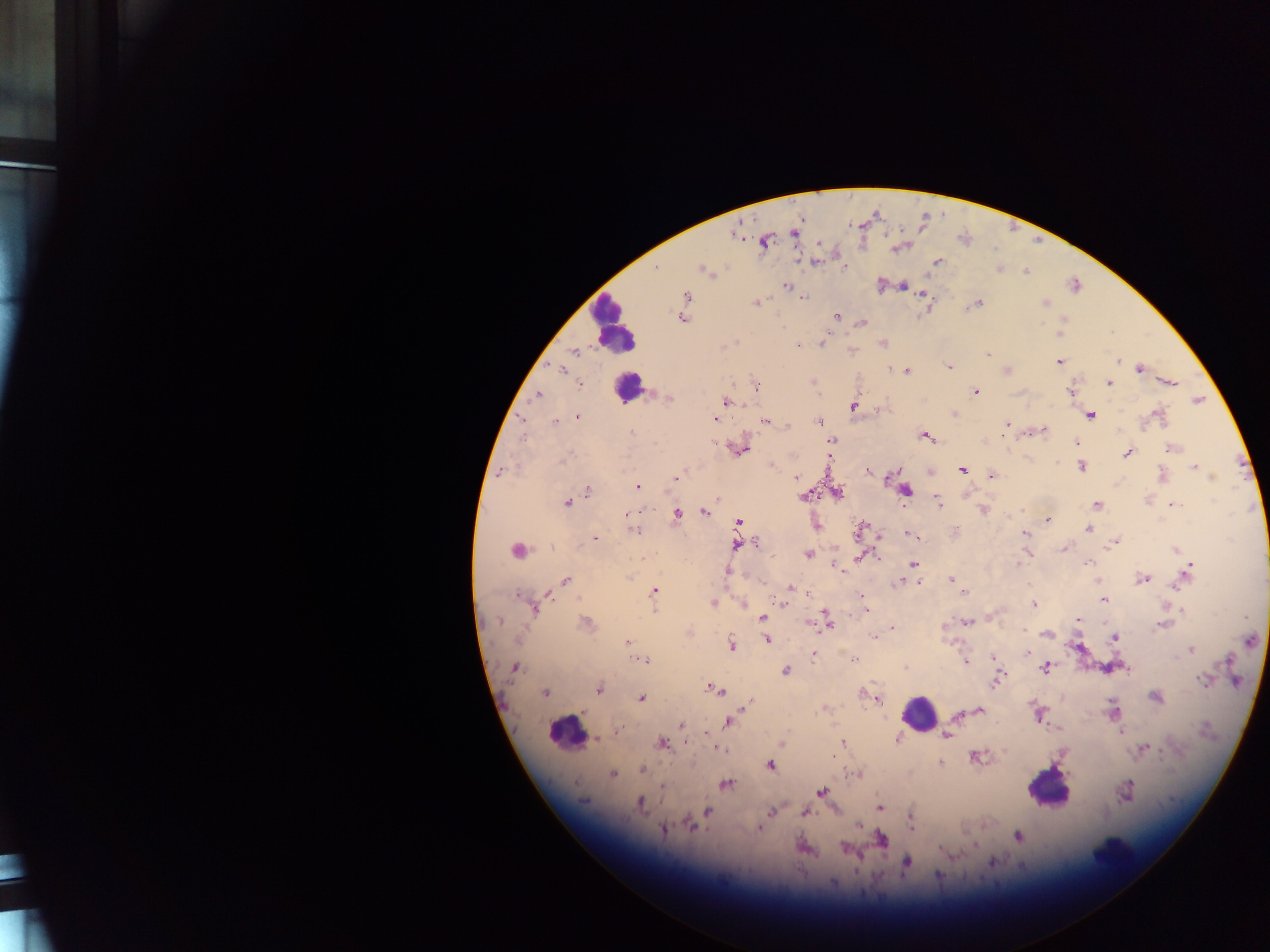

Approximate centers as (x, y) in pixels.
Summary:
  - Leukocyte locations: (613, 325), (628, 388), (919, 714), (565, 729), (1047, 788)
  - Plasmodium parasite locations: (794, 233), (764, 242), (897, 248), (815, 261), (937, 261), (844, 267), (657, 268), (704, 270), (1026, 271), (786, 286), (1076, 286), (904, 287), (923, 295), (686, 296), (804, 298), (755, 303), (978, 303), (1045, 303), (836, 316), (682, 318), (862, 323), (783, 327), (1059, 334), (733, 343), (882, 343), (822, 344), (797, 346), (723, 347), (852, 350), (575, 351), (987, 354), (1118, 362), (1058, 363), (948, 366), (1139, 368), (562, 369), (1006, 370), (907, 371), (813, 381), (1170, 381), (1109, 383), (580, 384), (756, 386), (1072, 390), (975, 392), (537, 394), (669, 398), (1197, 400), (727, 402), (854, 407), (955, 414), (1092, 415), (577, 416), (1158, 416), (522, 418), (715, 419), (819, 421), (555, 422), (767, 422), (787, 425), (1005, 427), (1043, 430), (632, 433), (1003, 433), (522, 436), (926, 436), (832, 441), (1076, 443), (1171, 448), (741, 449), (1127, 453), (831, 457), (564, 458), (1081, 467), (1193, 467), (867, 470), (963, 470), (502, 472), (1162, 474), (992, 476), (796, 477), (1212, 477), (676, 478), (638, 487), (906, 490), (588, 492), (839, 493), (803, 496), (717, 498), (937, 501), (567, 502), (1097, 505), (1173, 505), (983, 509), (704, 512), (676, 515), (1048, 521), (739, 522), (1088, 529), (633, 530), (858, 530), (1025, 533), (909, 534), (915, 536), (594, 538), (756, 543), (1114, 543), (735, 544), (1064, 549), (517, 550), (1176, 550), (808, 554), (864, 555), (913, 563), (1088, 563), (1018, 564), (1190, 566), (836, 567), (1188, 571), (727, 572), (628, 578), (565, 579), (950, 579), (1142, 579), (1097, 580), (919, 581), (899, 584), (790, 587), (654, 592), (965, 593), (549, 595), (861, 596), (518, 597), (1104, 600), (713, 603), (782, 603), (1033, 605), (534, 607), (1182, 610), (867, 611), (654, 612), (762, 616), (825, 616), (1077, 620), (499, 621), (827, 622), (967, 622), (586, 624), (1161, 626), (892, 628), (689, 633), (1046, 634), (874, 637), (1114, 638), (766, 639), (627, 641), (1251, 641), (732, 644), (1191, 650), (1028, 652), (814, 654), (855, 659), (994, 659), (645, 660), (965, 662), (1228, 662), (514, 668), (906, 668), (1045, 668), (1126, 668), (785, 671), (997, 680), (1203, 680), (598, 688), (708, 688), (716, 690), (544, 693), (641, 698), (1155, 698), (876, 699), (746, 705), (822, 710), (980, 710), (1112, 710), (957, 714), (1037, 714), (727, 722), (681, 725), (1121, 730), (615, 732), (705, 733), (946, 735), (598, 739), (898, 739), (843, 742), (661, 743), (783, 743), (718, 749), (1143, 749), (976, 757), (940, 763), (770, 765), (642, 770), (857, 774), (613, 775), (726, 784), (661, 786), (821, 792), (1126, 792), (583, 801), (640, 803), (879, 807), (708, 811), (772, 811), (805, 813), (911, 819), (692, 825), (858, 826), (664, 828), (759, 829), (1017, 835), (881, 839), (846, 848), (942, 849), (991, 862), (906, 863), (938, 876), (832, 883)
  - Country: Ghana
  - Capture: mobile-phone photograph through a microscope
  - Image size: 1270×952 pixels
  - Field of view: single
  - Preparation: thick blood smear